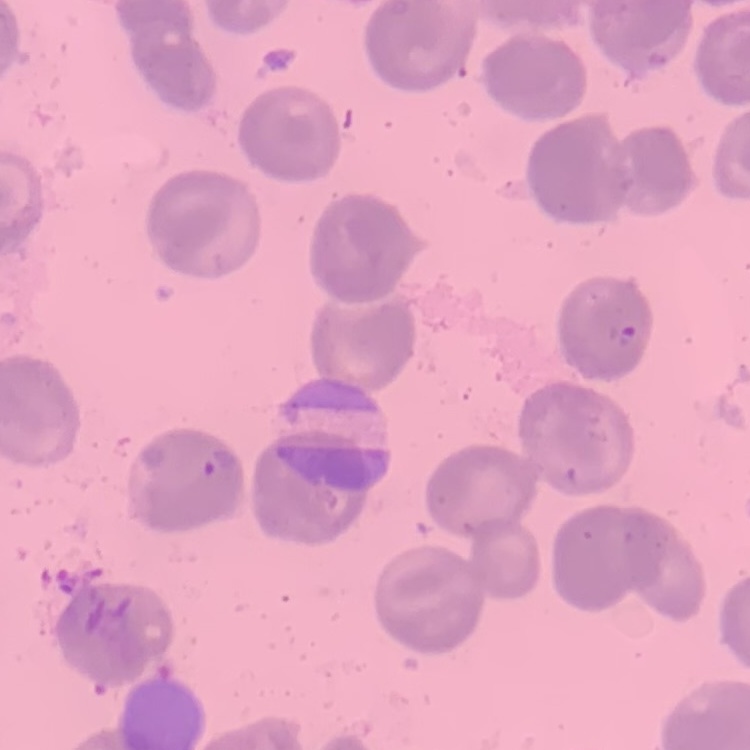 The red blood cells show no rouleaux formation. One tile cut from a larger photomicrograph. Thin blood film. Field's or Giemsa stain.